Report the malaria status of this cell.
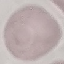

It is uninfected.

Thin smear of blood. Giemsa stain. Photographed with a smartphone camera at the microscope eyepiece. Cell patch, automatically extracted from a larger field of view and resized to 64 × 64 pixels.